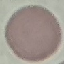

result = no malaria parasites detected
image type = automatically extracted cell patch, resized to 64 × 64 pixels
capture = smartphone through the microscope eyepiece
preparation = thin blood smear
stain = Giemsa